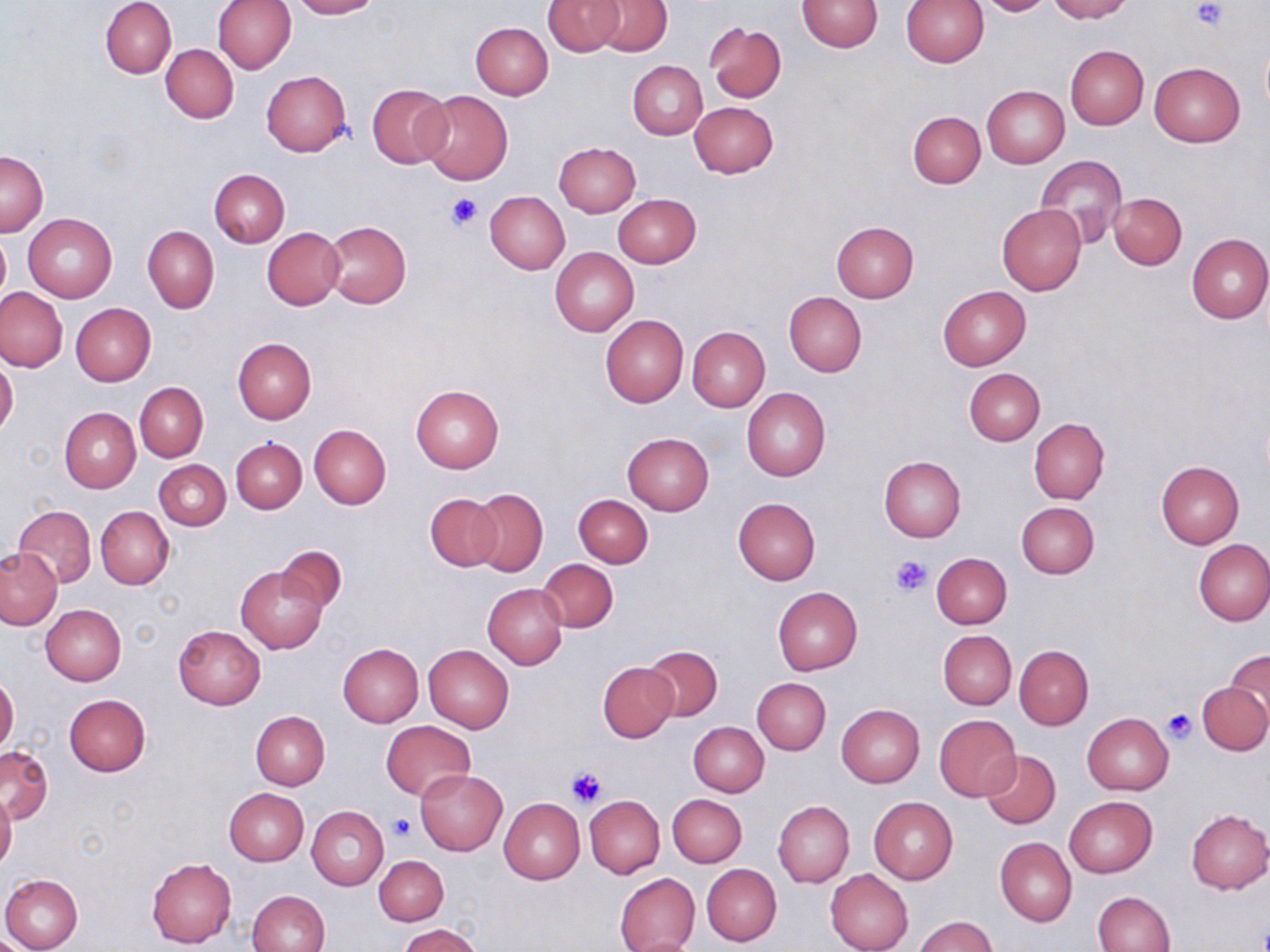
Summary:
  - Coordinate format: approximate bounding boxes as (x1, y1, x2, y2) in pixels
  - Uninfected red blood cell locations: (100, 0, 176, 78), (214, 0, 295, 74), (290, 0, 381, 19), (545, 0, 623, 55), (593, 0, 671, 55), (797, 0, 881, 53), (900, 0, 989, 66), (975, 0, 1053, 16), (1044, 0, 1132, 22), (470, 21, 553, 99), (704, 21, 787, 102), (161, 44, 238, 123), (1065, 45, 1148, 129), (628, 60, 707, 139), (1148, 62, 1244, 147), (261, 70, 352, 156), (367, 85, 452, 169), (982, 85, 1070, 168), (420, 90, 513, 185), (689, 102, 778, 178), (908, 111, 985, 188), (553, 142, 641, 217), (0, 151, 48, 236), (1036, 154, 1127, 249), (209, 168, 289, 247), (485, 191, 570, 274), (1108, 192, 1186, 269), (613, 194, 701, 267), (996, 204, 1087, 295), (23, 213, 116, 304), (323, 221, 411, 310), (830, 221, 919, 302), (142, 225, 219, 313), (262, 226, 346, 310), (0, 232, 10, 307), (1186, 233, 1269, 323), (550, 247, 638, 337), (939, 285, 1030, 370), (0, 287, 67, 371), (784, 292, 866, 376), (71, 303, 156, 385), (600, 315, 688, 408), (687, 327, 770, 412), (233, 338, 316, 423), (0, 357, 18, 437), (962, 368, 1045, 446), (135, 382, 208, 461), (411, 384, 504, 472), (742, 387, 831, 481), (59, 408, 139, 492), (1029, 418, 1109, 504), (308, 425, 391, 508), (623, 432, 713, 514), (231, 437, 306, 512), (879, 456, 966, 542), (155, 460, 230, 531), (1156, 461, 1245, 548), (467, 488, 548, 577), (425, 494, 503, 571), (574, 494, 653, 568), (733, 497, 821, 584), (1016, 501, 1099, 579), (13, 504, 97, 587), (95, 505, 175, 589), (1193, 539, 1270, 626), (276, 544, 347, 612), (0, 548, 61, 629), (931, 553, 1012, 628), (538, 559, 618, 633), (236, 565, 328, 654), (483, 584, 568, 669), (772, 586, 863, 675), (40, 604, 126, 686), (173, 625, 266, 710), (938, 630, 1016, 709), (337, 644, 424, 727), (424, 644, 513, 733), (642, 645, 722, 721), (1014, 645, 1093, 729), (1226, 650, 1270, 724), (598, 661, 677, 741), (0, 675, 19, 754), (752, 678, 830, 755), (1197, 682, 1270, 755), (64, 694, 151, 776), (835, 704, 924, 788), (250, 711, 329, 790), (1082, 713, 1174, 795), (933, 715, 1021, 801), (688, 721, 768, 796), (382, 722, 476, 800), (682, 722, 758, 866), (0, 745, 53, 825), (979, 750, 1060, 829), (415, 769, 508, 855), (224, 788, 308, 865), (0, 792, 17, 871), (668, 793, 747, 867), (585, 795, 665, 879), (1064, 796, 1157, 877), (869, 797, 958, 885), (499, 798, 585, 884), (773, 800, 853, 889), (306, 806, 388, 890), (1185, 809, 1269, 893), (996, 837, 1076, 926), (374, 856, 448, 925), (146, 858, 236, 947), (701, 863, 782, 946), (825, 869, 913, 952), (613, 872, 700, 952), (1, 873, 83, 952), (247, 890, 329, 952), (1093, 891, 1176, 952), (913, 915, 997, 952), (398, 925, 483, 952)
  - Platelet locations: (1190, 1, 1228, 33), (446, 192, 483, 231), (888, 553, 932, 597), (1162, 708, 1195, 743), (566, 765, 607, 808), (387, 813, 415, 841)
  - Slide-level diagnosis: no evidence of blood parasites
  - Modality: light microscopy
  - Image size: 1270×952 pixels
  - Preparation: thin blood film
  - Magnification: 1000x
  - Stain: May-Grünwald-Giemsa
  - Field of view: single